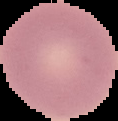

From a thin blood film. The area outside the segmented cell region is set to black. Image is 118×121 pixels. Result: negative for Plasmodium parasites.